Point out each leukocyte.
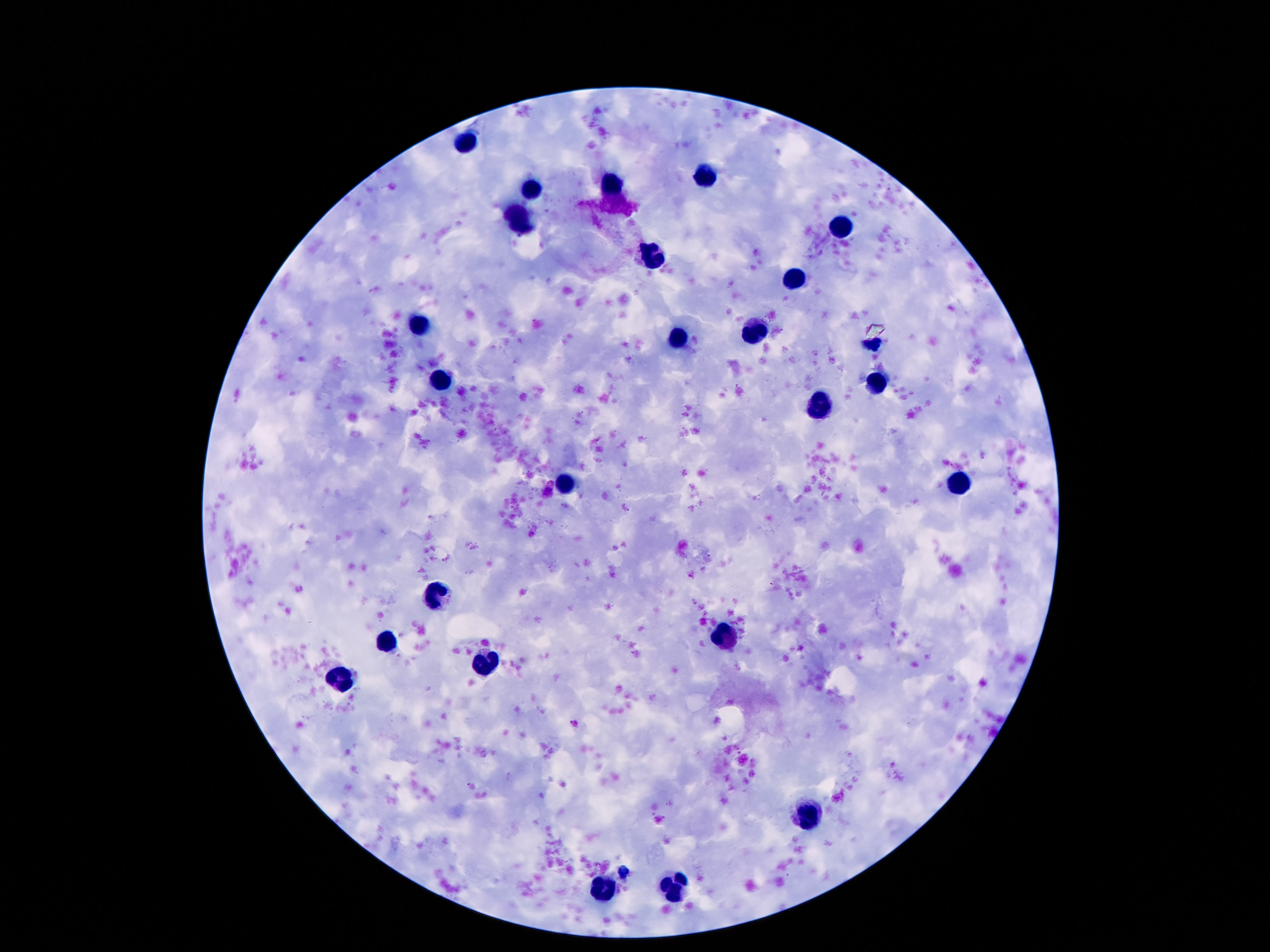
Approximate centers as (x, y) in pixels.
Leukocytes: (464, 141), (711, 172), (612, 186), (530, 188), (523, 219), (839, 228), (658, 259), (797, 279), (419, 327), (755, 332), (678, 339), (874, 341), (441, 380), (877, 386), (819, 403), (567, 482), (961, 483), (437, 597), (722, 635), (386, 642), (486, 666), (342, 677), (810, 814), (605, 887), (673, 887).

preparation = thick peripheral-blood smear
field of view = one from this slide
magnification = 100x
capture = smartphone camera through the microscope eyepiece
patient malaria status = not infected
stain = Giemsa
image size = 1270×952 pixels